Report the malaria status of this cell.
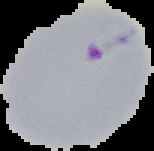

It is parasitized.

preparation = thin blood smear
image size = 154×151 pixels
image type = segmented cell region on a black background